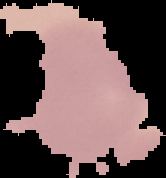

Result: negative for malaria parasites. From a thin blood smear. The area outside the segmented cell region is set to black. Image is 166×178 pixels.